Identify the blood parasite species.
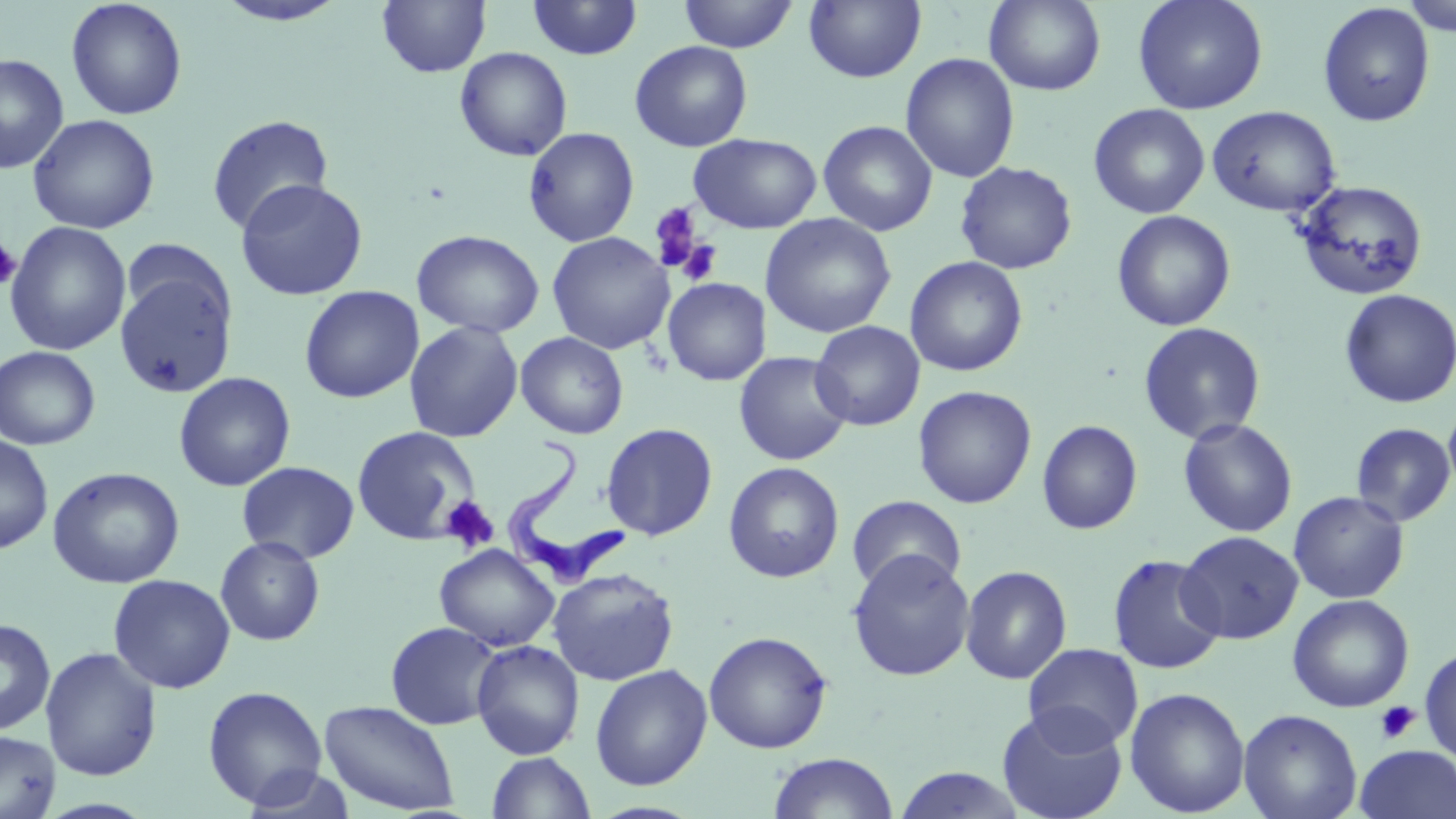

Trypanosoma brucei.

Approximate bounding boxes as (x1,y1)-(x2,y2) corner pairs in pixels. Uninfected red blood cell locations: (66,0)-(188,121), (212,0)-(351,27), (526,0)-(643,61), (677,0)-(799,52), (804,0)-(926,83), (983,0)-(1107,95), (1133,0)-(1268,115), (377,1)-(491,77), (1400,1)-(1456,38), (1317,2)-(1436,127), (630,40)-(753,152), (454,46)-(573,162), (900,52)-(1020,183), (0,53)-(69,174), (1088,103)-(1210,219), (1206,105)-(1341,217), (27,114)-(160,234), (206,114)-(334,235), (818,120)-(938,237), (523,126)-(640,247), (689,133)-(822,233), (955,161)-(1077,274), (235,178)-(368,301), (1293,179)-(1428,300), (1112,210)-(1236,332), (760,213)-(896,338), (5,221)-(132,355), (412,229)-(545,339), (547,231)-(674,354), (904,256)-(1028,377), (114,263)-(237,398), (662,277)-(771,385), (299,285)-(424,404), (1339,289)-(1455,409), (404,320)-(523,443), (810,320)-(925,431), (1138,322)-(1266,445), (515,331)-(629,439), (0,345)-(100,449), (734,351)-(853,466), (173,371)-(296,491), (913,385)-(1037,509), (1443,402)-(1456,497), (1178,417)-(1298,538), (1036,419)-(1143,535), (1351,422)-(1455,527), (601,423)-(718,541), (351,425)-(482,545), (0,434)-(54,554), (236,461)-(360,564), (723,461)-(845,583), (47,466)-(185,589), (1288,491)-(1410,604), (847,494)-(966,595), (1176,530)-(1303,644), (215,535)-(325,646), (434,543)-(559,652), (847,549)-(976,682), (1106,553)-(1226,674), (959,565)-(1072,685), (548,567)-(680,686), (108,574)-(235,693), (1287,594)-(1414,713), (0,618)-(56,735), (385,621)-(503,730), (703,630)-(832,754), (471,640)-(585,759), (1023,642)-(1144,751), (1419,645)-(1456,764), (41,646)-(162,782), (589,664)-(713,790), (202,685)-(328,810), (1124,687)-(1251,817), (318,699)-(460,816), (996,705)-(1128,819), (1238,708)-(1363,819), (0,730)-(61,819), (1355,744)-(1456,819), (487,752)-(596,819), (768,752)-(898,818), (891,766)-(1030,818). Platelet locations: (648,202)-(705,272), (0,236)-(22,291), (674,239)-(724,286), (439,495)-(499,553), (1376,701)-(1420,744). Trypanosoma brucei locations: (507,436)-(628,595). 1000x magnification. Optical microscopy. Thin blood film. Single field of view. May-Grünwald-Giemsa-stained preparation. Image is 1456×819 pixels.